Classify this cell by malaria status.
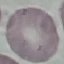

It is uninfected.

Summary:
  - Stain: Giemsa
  - Preparation: thin blood film
  - Image type: automatically extracted cell patch, resized to 64 × 64 pixels
  - Capture: smartphone through the microscope eyepiece